Report the malaria status of this cell.
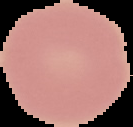

It is uninfected.

Summary:
  - Image type: segmented cell region with the area outside set to black
  - Preparation: thin blood smear
  - Image size: 133×127 pixels